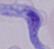 A trypanosome is shown. Photomicrograph. 1000x magnification.